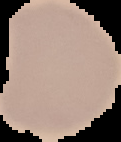
Image is 121×142 pixels. The area outside the segmented cell region is set to black. Malaria status: uninfected. From a thin blood smear.